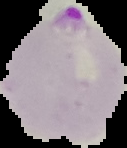

preparation = thin blood film
image size = 127×148 pixels
image type = segmented cell region on a black background
malaria status = parasitized